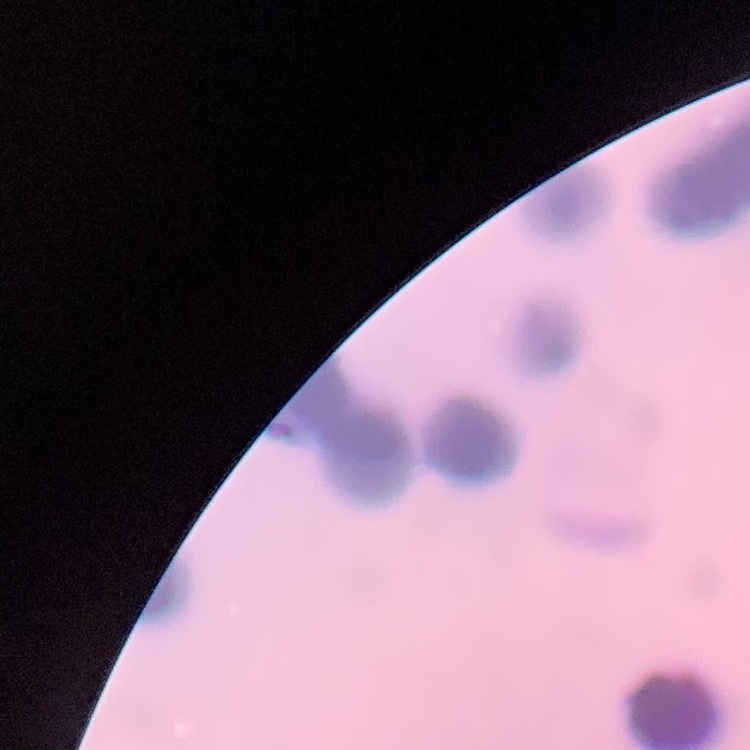
The erythrocytes exhibit rouleaux formation. One tile cut from a larger photomicrograph. Field's or Giemsa stain. Thin blood film.